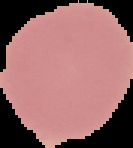
Cell region segmented out of the field of view; the surrounding area is masked to black. Image is 133×148 pixels. Result: no Plasmodium parasites detected. From a thin blood smear.